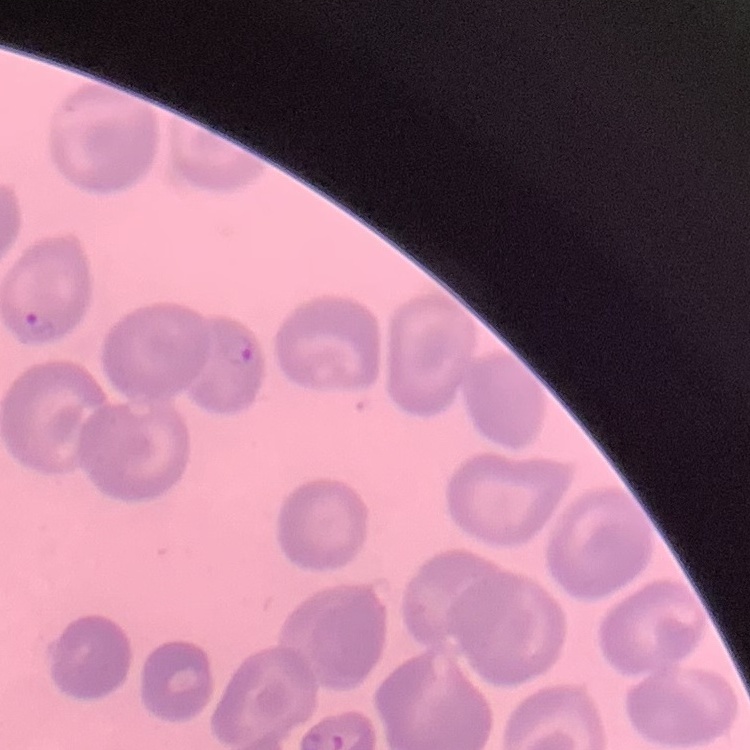 The red blood cells show no rouleaux formation. One tile cut from a larger photomicrograph. Thin blood smear. Field's or Giemsa stain.